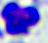 Captured at 400x magnification. A white blood cell is seen. Photomicrograph.